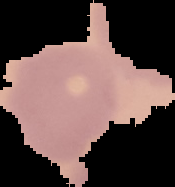
{
  "image_type": "segmented cell region on a black background",
  "image_size": "175×187 pixels",
  "malaria_status": "uninfected",
  "preparation": "thin blood film"
}